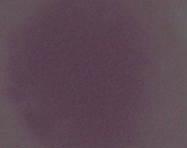

{
  "identification": "red blood cell",
  "modality": "photomicrograph",
  "magnification": "1000x"
}